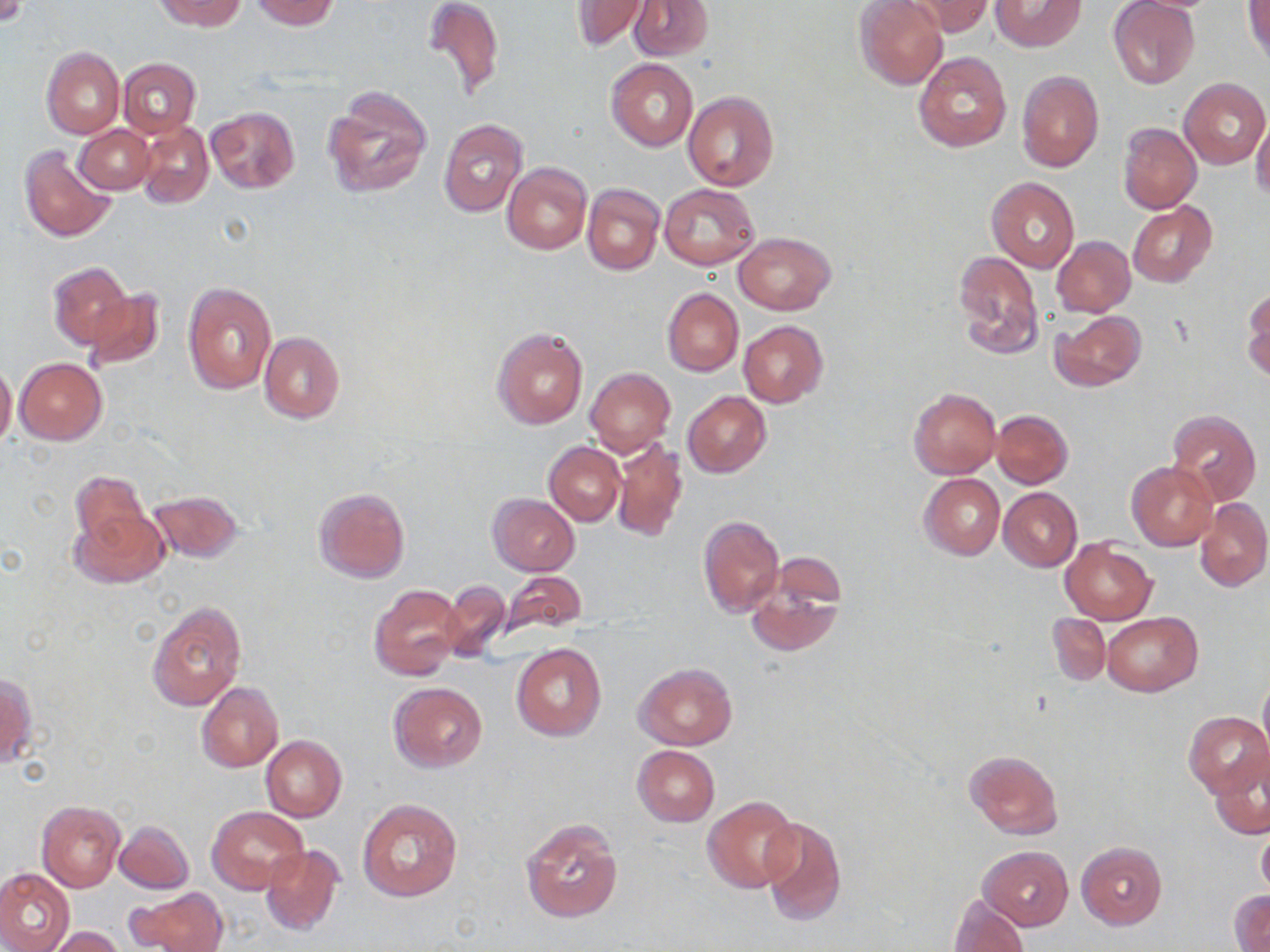

Approximate bounding boxes as (x1,y1)-(x2,y2) corner pairs in pixels. Uninfected red blood cell locations: (153,0)-(247,30), (423,0)-(504,99), (629,0)-(713,60), (855,0)-(948,90), (904,0)-(994,37), (990,0)-(1085,51), (1108,0)-(1201,89), (249,1)-(340,30), (570,1)-(648,52), (1244,1)-(1270,65), (42,47)-(125,138), (913,51)-(1012,152), (118,58)-(200,138), (607,58)-(697,152), (1016,70)-(1103,172), (1181,77)-(1270,168), (321,85)-(433,199), (682,91)-(779,191), (205,107)-(300,193), (438,117)-(527,218), (1251,117)-(1270,202), (137,122)-(214,209), (1118,122)-(1201,214), (74,125)-(155,194), (18,145)-(117,242), (502,163)-(591,255), (987,176)-(1079,274), (583,183)-(664,276), (660,184)-(759,269), (1129,203)-(1217,287), (735,232)-(835,315), (1052,236)-(1135,318), (954,252)-(1045,361), (48,261)-(131,348), (182,283)-(277,393), (662,288)-(743,376), (84,289)-(163,371), (1243,289)-(1270,380), (1049,310)-(1146,390), (738,320)-(828,407), (491,327)-(588,430), (260,332)-(345,423), (14,358)-(106,444), (0,361)-(16,449), (585,368)-(675,456), (909,388)-(1001,478), (682,391)-(771,478), (991,409)-(1073,489), (1165,409)-(1261,508), (612,438)-(688,543), (545,442)-(624,527), (1126,461)-(1217,551), (70,470)-(148,548), (919,473)-(1005,560), (314,487)-(410,583), (998,487)-(1082,571), (148,490)-(242,563), (488,494)-(581,576), (1194,497)-(1270,591), (69,507)-(169,589), (697,514)-(784,617), (1060,539)-(1156,625), (745,565)-(845,658), (499,571)-(587,636), (441,581)-(509,661), (369,585)-(464,681), (147,601)-(246,710), (1048,613)-(1110,686), (1103,613)-(1202,695), (512,644)-(606,742), (634,663)-(738,750), (1,673)-(36,770), (1259,674)-(1270,757), (197,681)-(283,772), (389,682)-(488,771), (1184,710)-(1269,799), (260,735)-(346,821), (632,746)-(719,826), (965,750)-(1063,839), (1209,753)-(1269,841), (703,795)-(801,894), (357,799)-(462,903), (37,801)-(126,892), (207,806)-(308,895), (759,815)-(847,926), (520,817)-(622,923), (115,820)-(194,894), (1257,825)-(1270,899), (1077,841)-(1167,928), (260,843)-(344,935), (981,847)-(1072,928), (0,868)-(74,952), (132,888)-(228,952), (1229,891)-(1270,951), (947,893)-(1028,952), (49,926)-(125,952). Slide-level diagnosis: no evidence of blood parasites. Image is 1270×952 pixels. Optical microscopy. Thin blood film. One field of a larger specimen. May-Grünwald-Giemsa stain. Captured at 1000x magnification.